Classify this cell by malaria status.
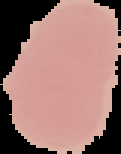

Uninfected.

preparation = thin blood smear
image type = segmented cell region on a black background
image size = 121×154 pixels